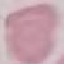
Summary:
  - Result: negative for malaria parasites
  - Image type: cell patch, automatically extracted from a larger field of view and resized to 64 × 64 pixels
  - Stain: Giemsa
  - Preparation: thin smear
  - Capture: smartphone through the microscope eyepiece